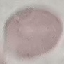
result: no malaria parasites detected
preparation: thin blood smear
stain: Giemsa
image_type: cell patch, automatically extracted from a larger field of view and resized to 64 × 64 pixels
capture: smartphone through the microscope eyepiece